State which parasite is depicted.
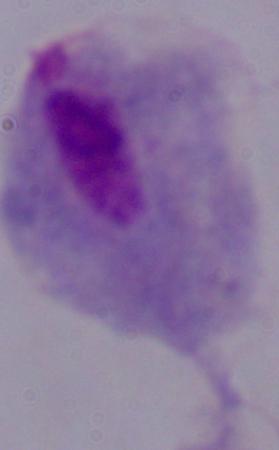

A trichomonad.

magnification: 1000x
modality: micrograph